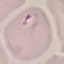
Summary:
  - Malaria status: parasitized
  - Image type: automatically extracted cell patch, resized to 64 × 64 pixels
  - Stain: Giemsa
  - Capture: smartphone camera at the microscope eyepiece
  - Preparation: thin smear